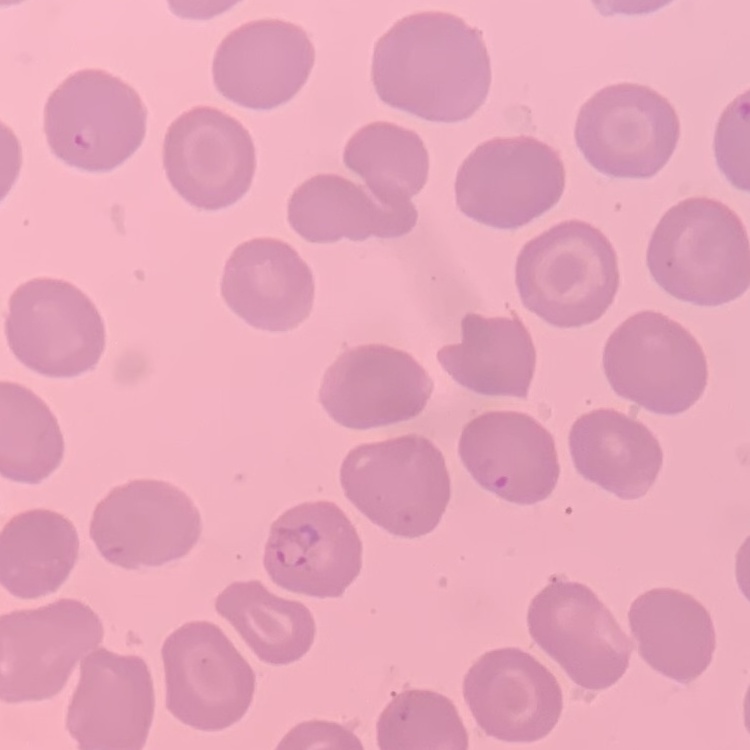

The erythrocytes exhibit no rouleaux formation. Thin blood smear. Field's or Giemsa stain. Square crop of a larger photomicrograph.